Describe the morphology of the erythrocytes.
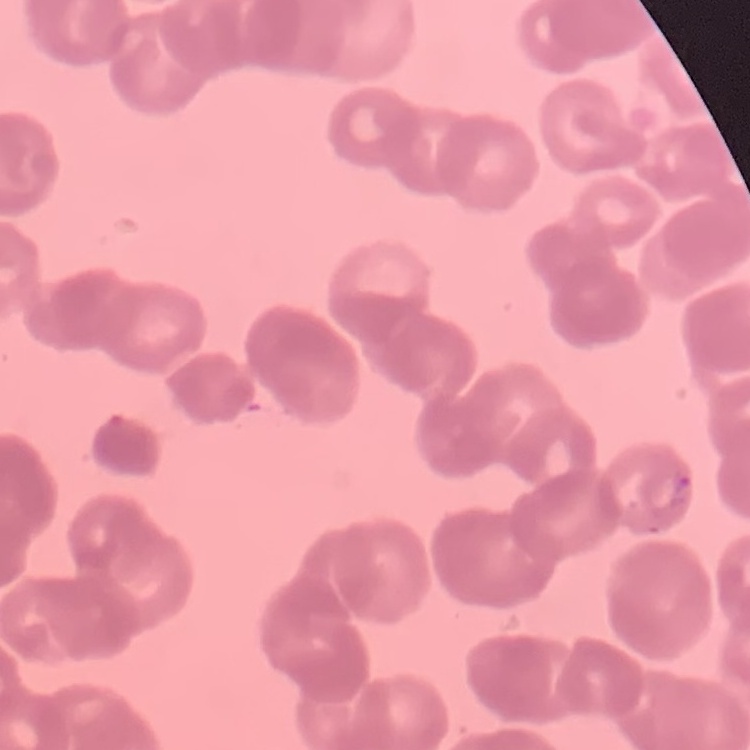
They show rouleaux formation.

preparation: thin blood smear
image_type: square crop of a larger photomicrograph
stain: Field's or Giemsa